Give the position of every leukocyte visible.
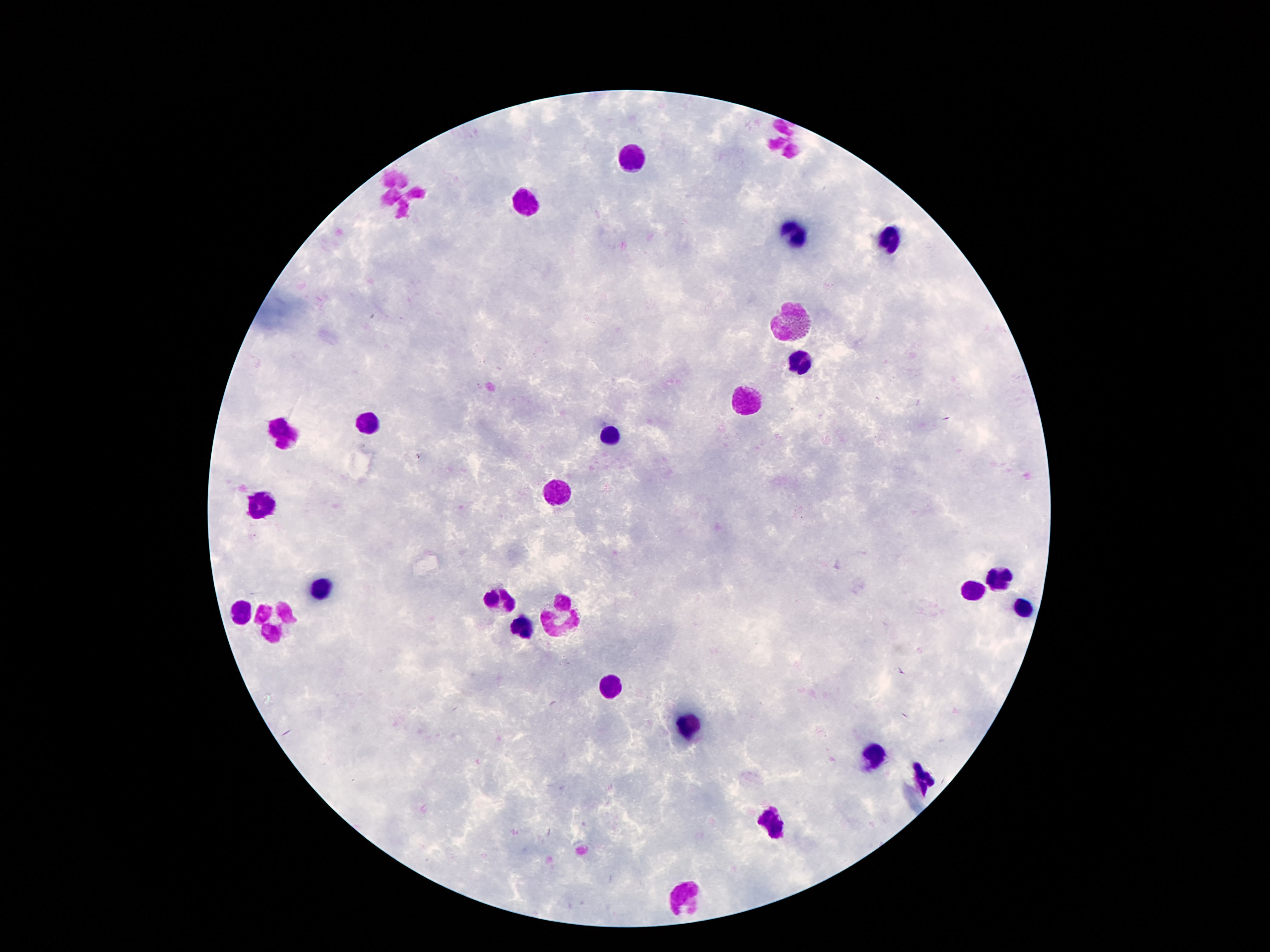

Approximate centers as (x, y) in pixels.
Leukocytes: (789, 139), (633, 155), (399, 195), (525, 203), (795, 233), (891, 239), (793, 322), (799, 363), (745, 399), (367, 420), (283, 431), (611, 439), (553, 493), (261, 502), (999, 581), (325, 588), (973, 591), (497, 600), (1021, 609), (241, 610), (565, 613), (275, 618), (521, 624), (617, 690), (687, 728), (873, 755), (923, 781), (777, 825), (681, 893).

Summary:
  - Field of view: single
  - Preparation: thick blood film
  - Patient malaria status: not infected
  - Image size: 1270×952 pixels
  - Capture: smartphone camera through the microscope eyepiece
  - Stain: Giemsa
  - Magnification: 100x